Assess for Plasmodium parasites.
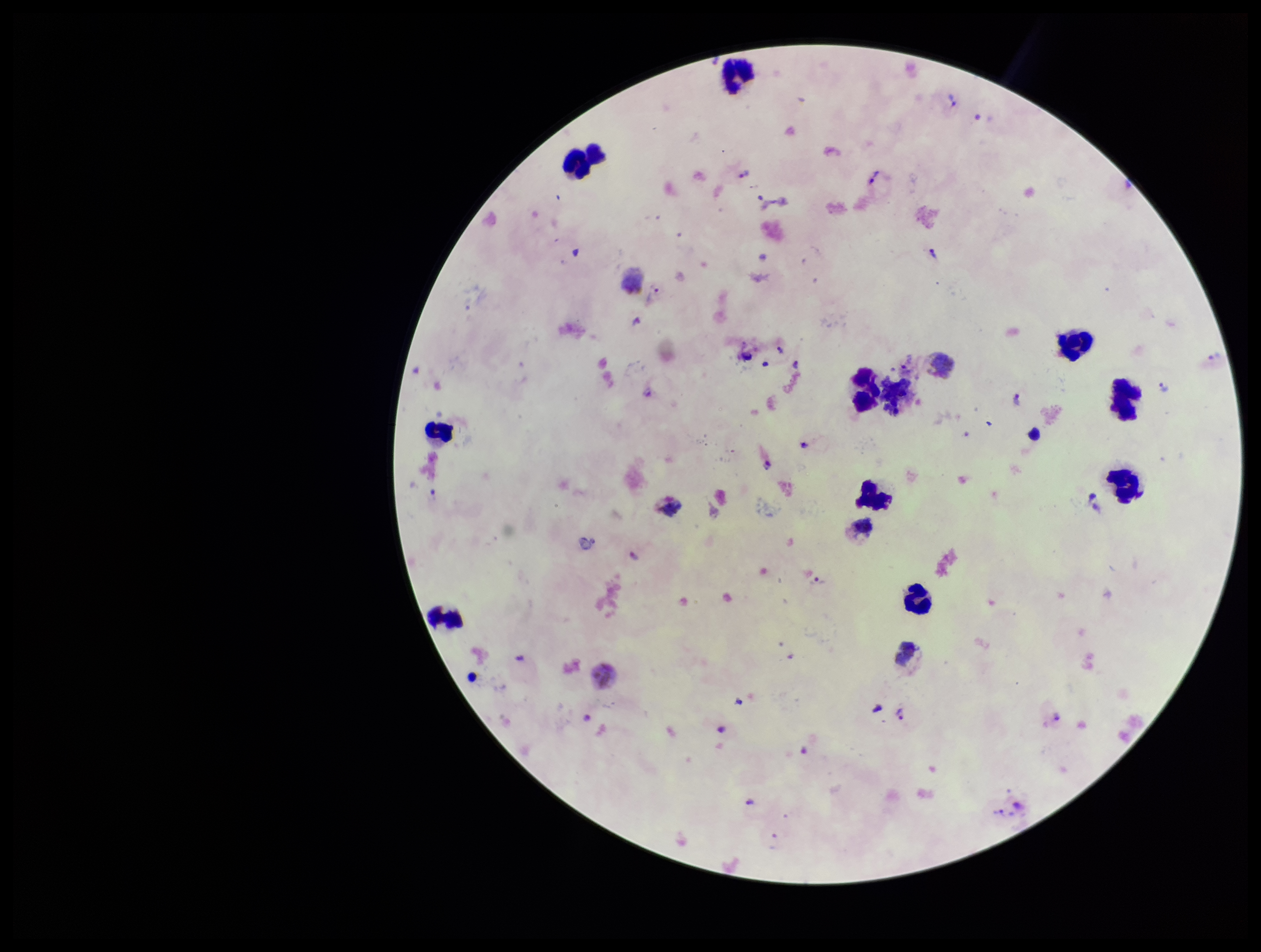

Identified.

Image is 1261×952 pixels. Species reported for this patient: Plasmodium vivax. Leukocyte count: 14. Parasite count: 17. Stained with Giemsa. Single field of view. Smartphone photograph taken through the eyepiece of a microscope. Patient malaria status: positive. Preparation: thick smear.